Give a bounding box for every malaria parasite, every leukocyte, and every artifact (stain precipitate or debris).
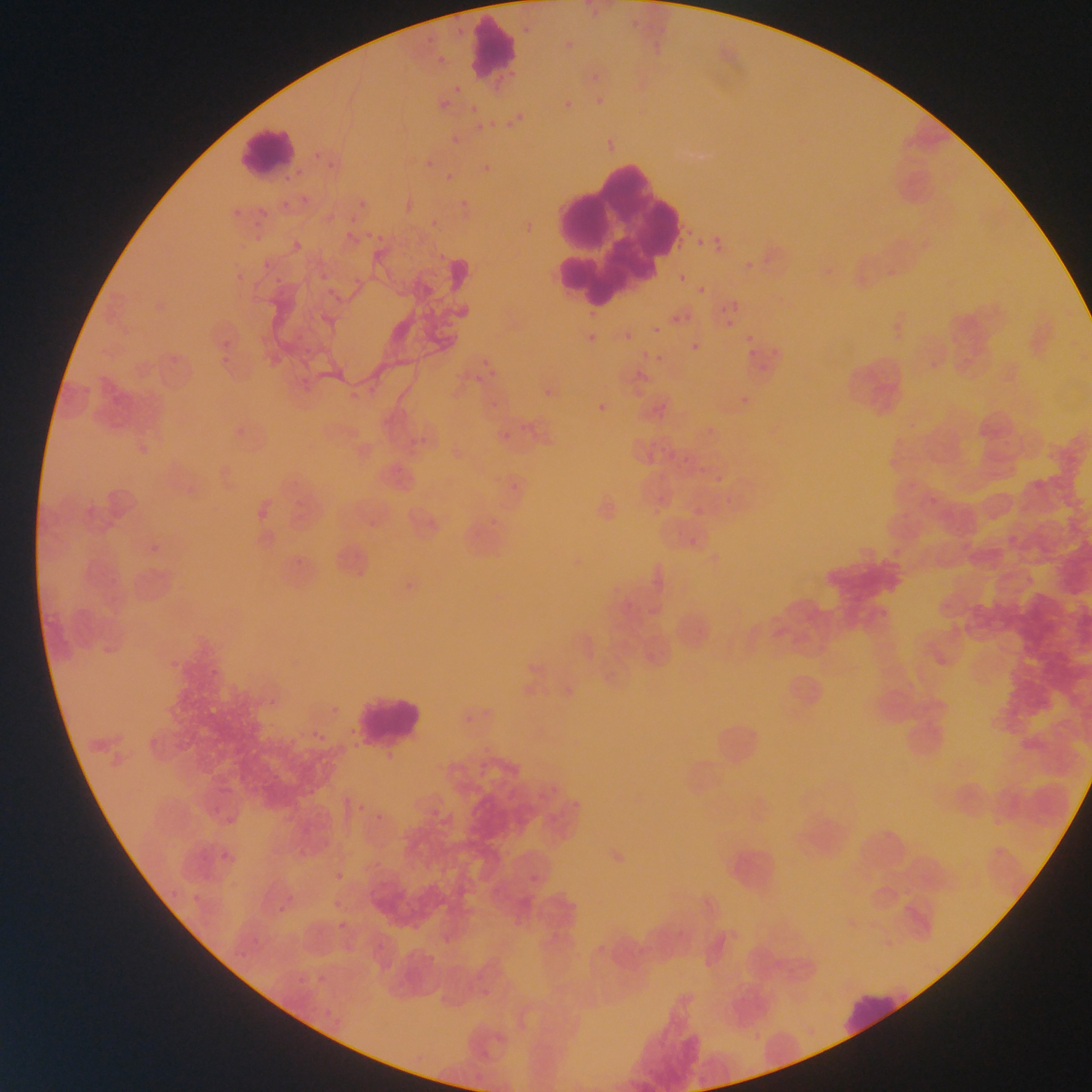
Approximate bounding boxes as {left, top, right, bottom} in pixels.
Malaria parasites: {520, 19, 537, 38}, {423, 32, 437, 46}, {433, 56, 445, 65}, {453, 83, 459, 96}, {562, 98, 571, 108}, {507, 107, 524, 120}, {489, 119, 496, 128}, {504, 123, 519, 133}, {444, 140, 455, 149}, {308, 142, 325, 159}, {322, 159, 339, 172}, {477, 159, 493, 173}, {418, 160, 431, 171}, {439, 170, 453, 184}, {296, 190, 317, 208}, {357, 195, 371, 211}, {457, 197, 466, 211}, {348, 217, 357, 225}, {363, 228, 375, 241}, {254, 236, 274, 252}, {697, 238, 706, 246}, {293, 243, 305, 252}, {715, 246, 722, 254}, {679, 274, 687, 283}, {696, 286, 705, 296}, {732, 301, 740, 311}, {583, 308, 594, 322}, {670, 316, 680, 324}, {725, 320, 733, 328}, {652, 326, 661, 334}, {214, 327, 233, 351}, {746, 334, 754, 342}, {623, 335, 632, 343}, {585, 337, 594, 346}, {691, 343, 700, 352}, {480, 349, 486, 362}, {650, 352, 659, 361}, {217, 355, 231, 367}, {481, 374, 498, 385}, {743, 396, 751, 404}, {595, 407, 606, 414}, {929, 496, 939, 506}, {359, 797, 368, 812}, {376, 814, 387, 823}, {335, 872, 348, 878}, {288, 889, 296, 901}, {334, 896, 349, 907}, {275, 901, 284, 912}, {338, 917, 346, 934}, {315, 971, 324, 990}.
Leukocytes: {467, 16, 518, 84}, {235, 125, 298, 176}, {546, 143, 676, 310}, {353, 691, 425, 746}, {833, 986, 915, 1035}.

Mobile-phone photograph taken through the microscope. One field of view. Image is 1092×1092 pixels. Thin blood smear. Sample from Ghana.